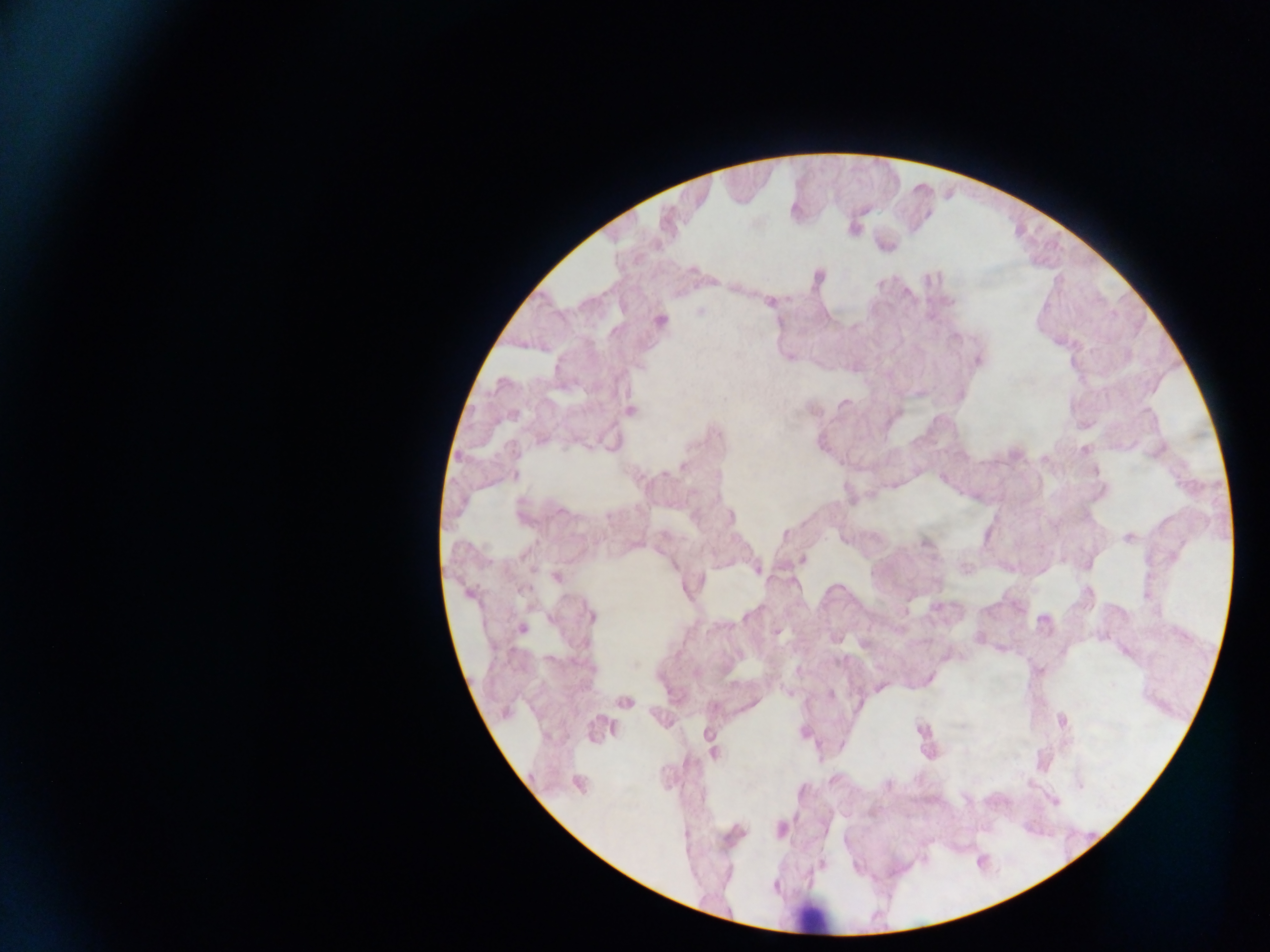
image size = 1270×952 pixels
leukocyte locations = approximate centers as x y in pixels: 812 916
field of view = single
country = Ghana
capture = mobile-phone photograph through a microscope
preparation = thick blood smear
malaria parasite locations = approximate centers as x y in pixels: 817 278; 770 302; 700 311; 661 320; 976 359; 629 411; 513 475; 1129 537; 924 542; 802 559; 757 569; 556 576; 590 614; 521 628; 928 679; 879 687; 829 694; 624 701; 1060 720; 598 729; 713 752; 578 783; 1053 799; 780 829